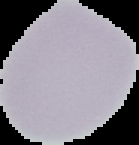
Summary:
  - Preparation: thin blood smear
  - Image type: cell region segmented out of the field of view; surrounding area masked to black
  - Image size: 139×145 pixels
  - Malaria status: uninfected